Report the malaria status of this cell.
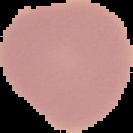

It is uninfected.

image type = cell region segmented out of the field of view; surrounding area masked to black
image size = 133×133 pixels
preparation = thin blood smear